Locate the P. falciparum-infected red blood cells and any of indeterminate infection status.
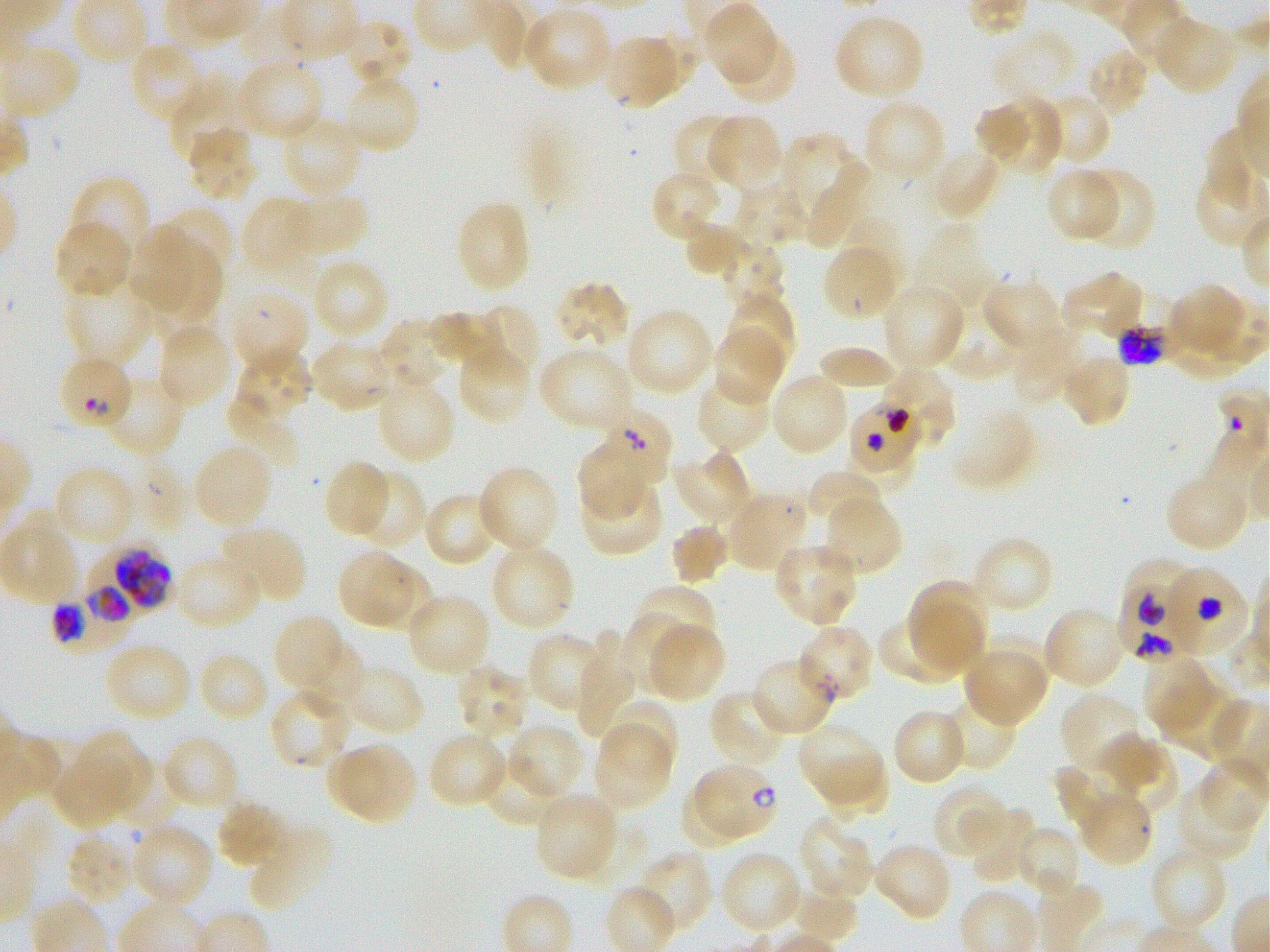
Approximate bounding boxes as [x1, y1, x2, y2] in pixels. Not every red blood cell is marked. A life-cycle stage — or a range of stages, where the recorded stages span more than one — follows each staged infected red blood cell.
Infected red blood cells: [602, 412, 670, 487]; [79, 545, 171, 623]; [1123, 560, 1200, 637]; [1166, 568, 1248, 651]; [49, 581, 130, 661]; [1117, 582, 1201, 665]; [796, 623, 875, 704]; [693, 762, 780, 840] ring.
Red blood cells of indeterminate infection status: [1118, 294, 1184, 366], [56, 353, 134, 434], [872, 366, 956, 452], [850, 399, 922, 470].

locations_of_uninfected_red_blood_cells: '[703, 2, 782, 89], [522, 6, 614, 92], [833, 12, 926, 102], [1152, 15, 1239, 97], [337, 19, 412, 88], [607, 36, 678, 112], [722, 38, 797, 105], [128, 41, 208, 126], [1085, 48, 1150, 116], [236, 57, 325, 141], [338, 72, 420, 157], [169, 79, 252, 167], [1035, 91, 1112, 166], [992, 95, 1064, 176], [861, 97, 948, 184], [973, 103, 1033, 164], [672, 114, 749, 190], [704, 114, 782, 192], [281, 115, 365, 199], [187, 127, 259, 202], [1207, 129, 1252, 214], [780, 136, 851, 211], [929, 145, 1003, 220], [809, 158, 872, 246], [1045, 167, 1124, 243], [1080, 167, 1156, 250], [649, 168, 725, 241], [68, 176, 151, 265], [733, 182, 806, 248], [291, 188, 370, 257], [244, 198, 318, 270], [456, 199, 532, 294], [157, 206, 235, 285], [679, 213, 750, 278], [843, 217, 908, 289], [54, 219, 134, 300], [129, 224, 192, 312], [153, 239, 223, 327], [716, 240, 784, 312], [823, 244, 898, 320], [309, 257, 390, 340], [1061, 269, 1145, 340], [982, 277, 1062, 345], [62, 279, 153, 366], [553, 281, 630, 354], [1173, 283, 1241, 348], [879, 284, 966, 373], [228, 287, 309, 375], [941, 293, 1019, 381], [727, 298, 796, 371], [464, 304, 538, 386], [624, 307, 716, 397], [429, 311, 508, 371], [1160, 312, 1250, 378], [374, 319, 453, 394], [155, 322, 232, 410], [711, 327, 785, 406], [1010, 330, 1082, 403], [310, 339, 395, 412], [456, 341, 532, 424], [537, 345, 635, 435], [816, 346, 898, 393], [239, 348, 313, 420], [1058, 351, 1131, 428], [103, 371, 189, 457], [770, 371, 851, 456], [696, 373, 773, 454], [376, 376, 456, 465], [227, 392, 304, 462], [949, 409, 1039, 490], [191, 442, 273, 531], [578, 445, 648, 519], [670, 450, 752, 531], [835, 454, 916, 494], [323, 459, 393, 539], [52, 464, 137, 547], [476, 465, 561, 554], [1165, 467, 1248, 552], [349, 468, 426, 549], [806, 470, 886, 540], [579, 476, 663, 556], [422, 491, 500, 567], [725, 491, 810, 574], [821, 493, 902, 576], [1, 515, 81, 606], [218, 523, 307, 606], [671, 524, 728, 585], [972, 535, 1054, 615], [773, 540, 860, 626], [488, 541, 575, 633], [335, 547, 415, 628], [173, 552, 263, 630], [366, 563, 435, 638], [908, 581, 990, 668], [636, 586, 718, 659], [405, 593, 492, 678], [912, 603, 984, 672], [1041, 605, 1127, 691], [615, 611, 692, 694], [878, 613, 971, 686], [272, 614, 342, 689], [645, 620, 725, 704], [575, 630, 639, 739], [525, 632, 609, 714], [977, 633, 1051, 704], [299, 637, 367, 715], [104, 639, 193, 722], [197, 650, 270, 723], [961, 654, 1043, 728], [751, 655, 838, 738], [1142, 656, 1220, 739], [457, 664, 530, 741], [346, 668, 424, 737], [1158, 677, 1246, 762], [268, 689, 350, 771], [708, 690, 791, 772], [939, 692, 1019, 772], [1059, 692, 1150, 778], [605, 698, 677, 773], [891, 707, 969, 786], [592, 720, 673, 812], [795, 720, 881, 803], [504, 721, 587, 802], [76, 731, 152, 809], [426, 731, 508, 809], [161, 734, 241, 813], [1096, 734, 1164, 791], [1099, 741, 1179, 815], [327, 743, 388, 815], [344, 743, 419, 826], [53, 752, 133, 829], [820, 752, 890, 820], [486, 755, 558, 824], [1196, 757, 1270, 835], [1056, 765, 1132, 833], [932, 780, 1009, 860], [680, 783, 747, 853], [1172, 783, 1257, 861], [533, 792, 620, 881], [1086, 795, 1154, 867], [215, 798, 288, 868], [964, 804, 1038, 885], [796, 814, 876, 903], [129, 821, 214, 910], [247, 824, 334, 911], [1013, 826, 1083, 898], [66, 829, 139, 910], [872, 840, 954, 922], [1148, 843, 1229, 932], [634, 849, 712, 937], [718, 850, 804, 936], [788, 885, 859, 944]'
donor_blood_group: O+
preparation: thin blood smear
objective: 100x, oil immersion, numerical aperture 1.25
culture: P. falciparum strain 3D7, static, in vitro
image_size: 1270×952 pixels
stain: Giemsa
field_of_view: single